Describe the morphology of the red blood cells.
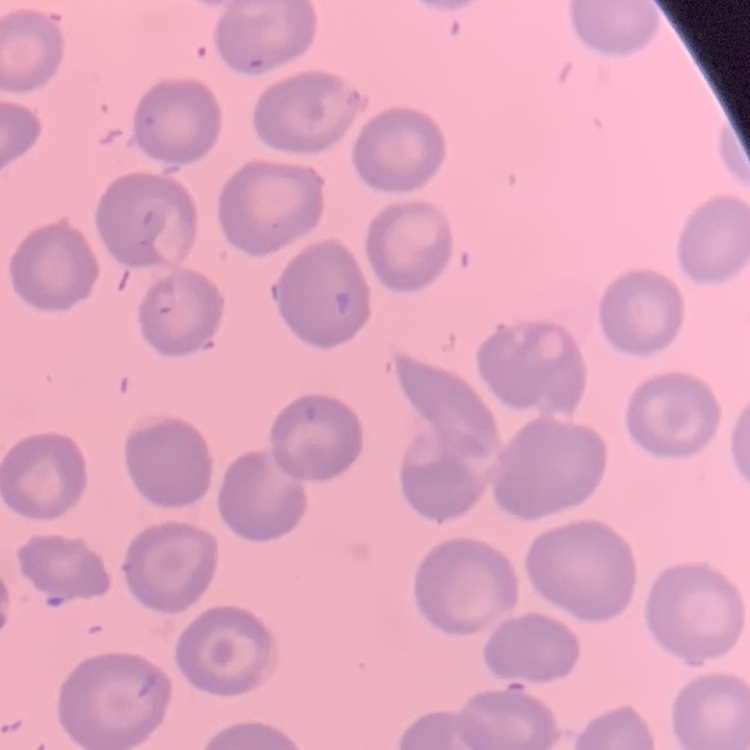

They show no rouleaux formation.

Square crop of a larger photomicrograph. Thin peripheral smear. Stained with either Field's or Giemsa.